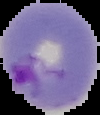
{
  "image_type": "segmented cell region on a black background",
  "image_size": "100×115 pixels",
  "preparation": "thin blood film",
  "result": "malaria parasites detected"
}